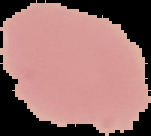

{
  "preparation": "thin blood film",
  "image_type": "cell region segmented out of the field of view; surrounding area masked to black",
  "image_size": "151×136 pixels",
  "malaria_status": "uninfected"
}